Point out each Plasmodium parasite.
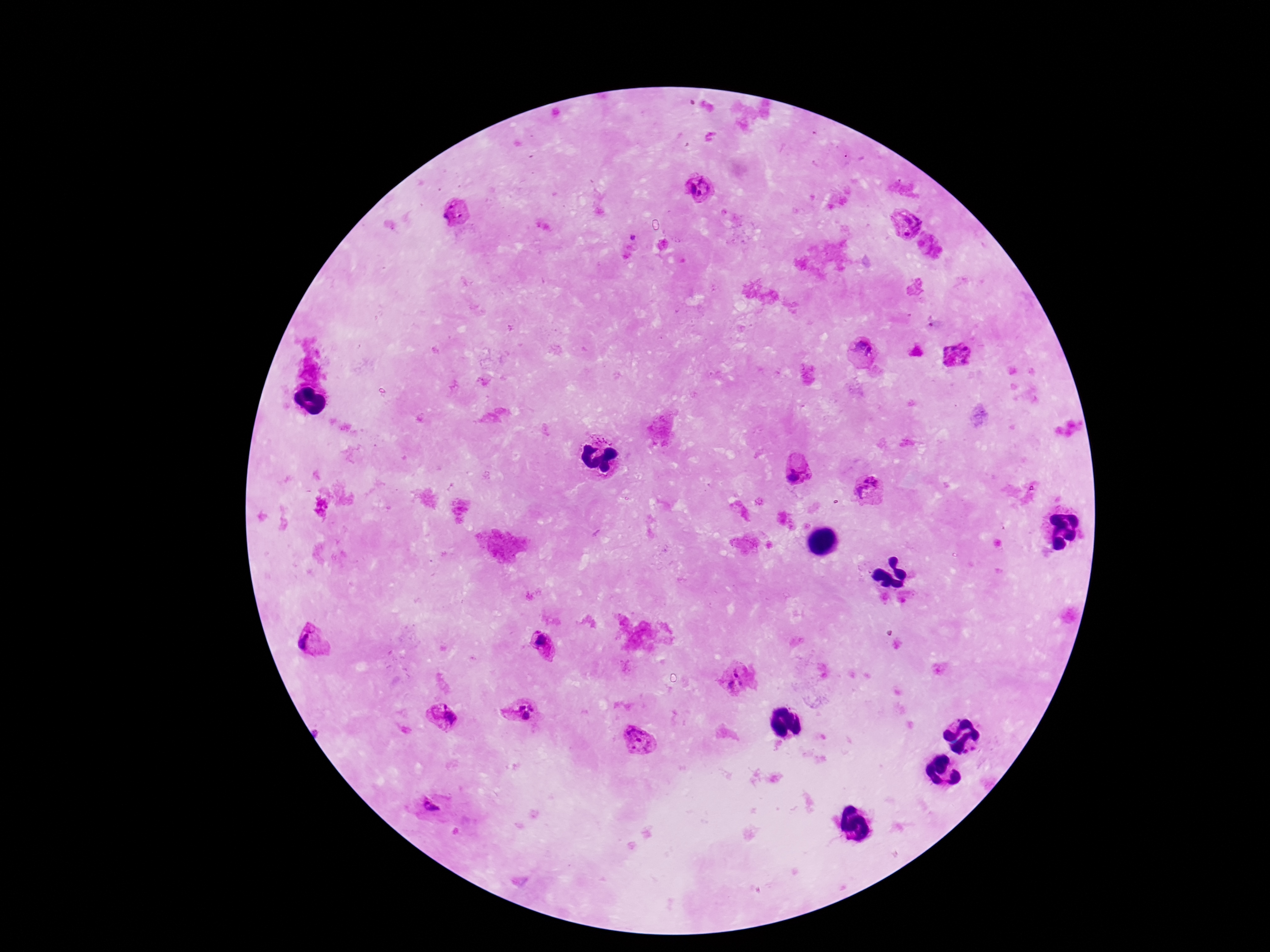

Approximate object centers, in pixels from the top-left corner.
Plasmodium parasites: (x=698, y=189), (x=455, y=212), (x=902, y=221), (x=930, y=246), (x=864, y=346), (x=958, y=353), (x=798, y=472), (x=870, y=490), (x=313, y=638), (x=543, y=647), (x=739, y=677), (x=522, y=709), (x=444, y=718), (x=638, y=742), (x=431, y=807).

Summary:
  - Magnification: 100x
  - Image size: 1270×952 pixels
  - Preparation: thick peripheral-blood smear
  - Field of view: single
  - Capture: smartphone camera through the microscope eyepiece
  - Patient malaria status: infected
  - Stain: Giemsa